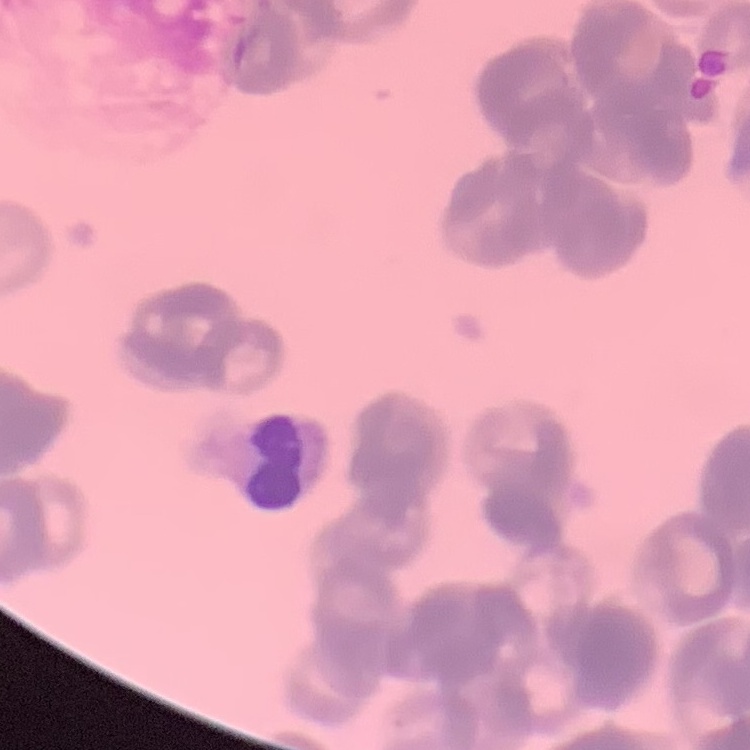

The red blood cells show rouleaux formation. Square crop of a larger photomicrograph. Stained with either Field's or Giemsa. Thin blood film.